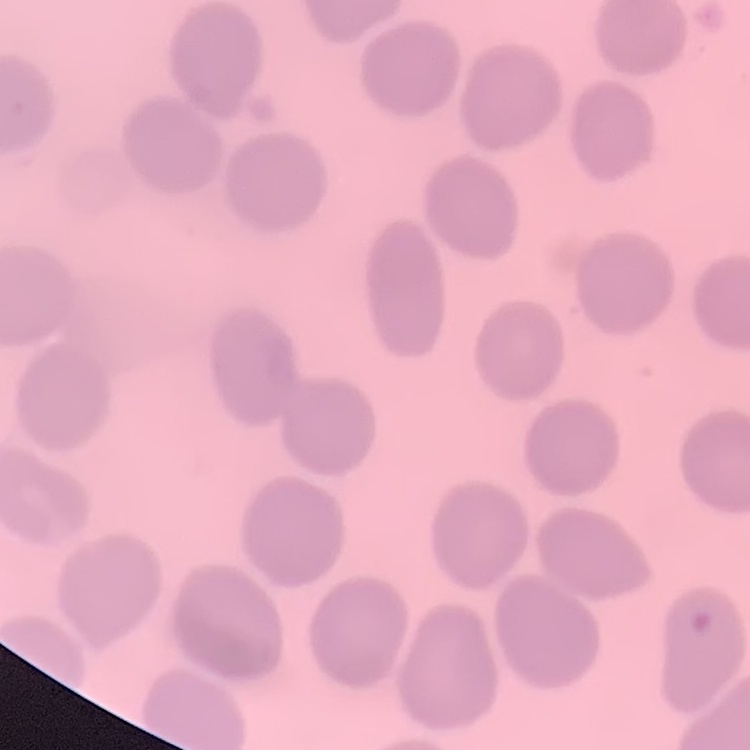
The red blood cells exhibit no rouleaux formation. Thin blood smear. One tile cut from a larger photomicrograph. Stained with either Field's or Giemsa.